Name the cell type shown.
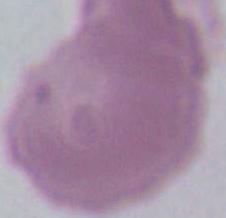
This is an erythrocyte.

1000x magnification. Micrograph.